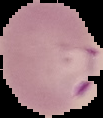
malaria status = parasitized
preparation = thin blood film
image type = segmented cell region with the area outside set to black
image size = 103×118 pixels